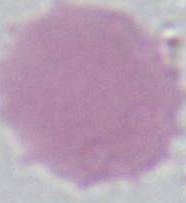
identification = erythrocyte
modality = photomicrograph
magnification = 1000x